Assess the morphology of the red blood cells.
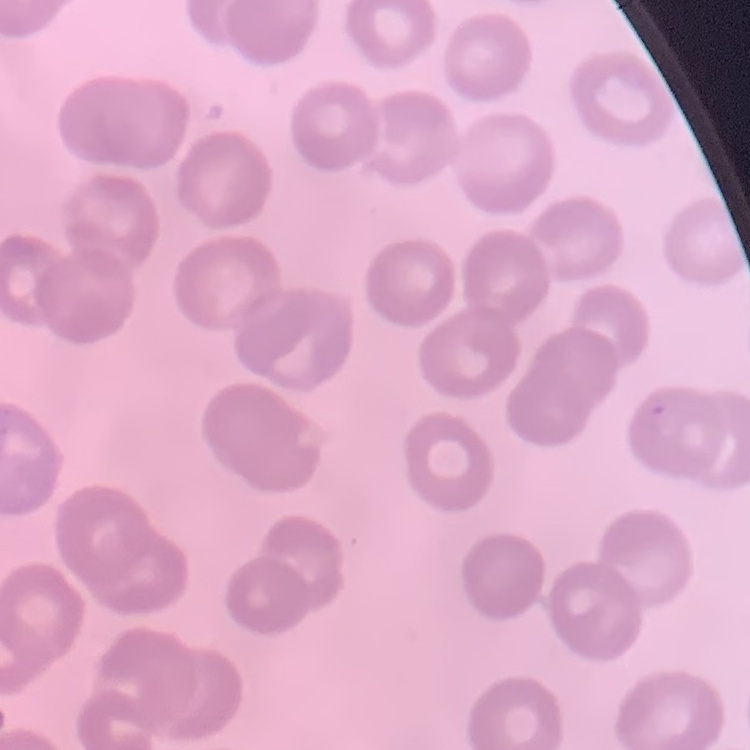

No rouleaux formation.

Thin blood smear. Square crop of a larger photomicrograph. Field's or Giemsa stain.